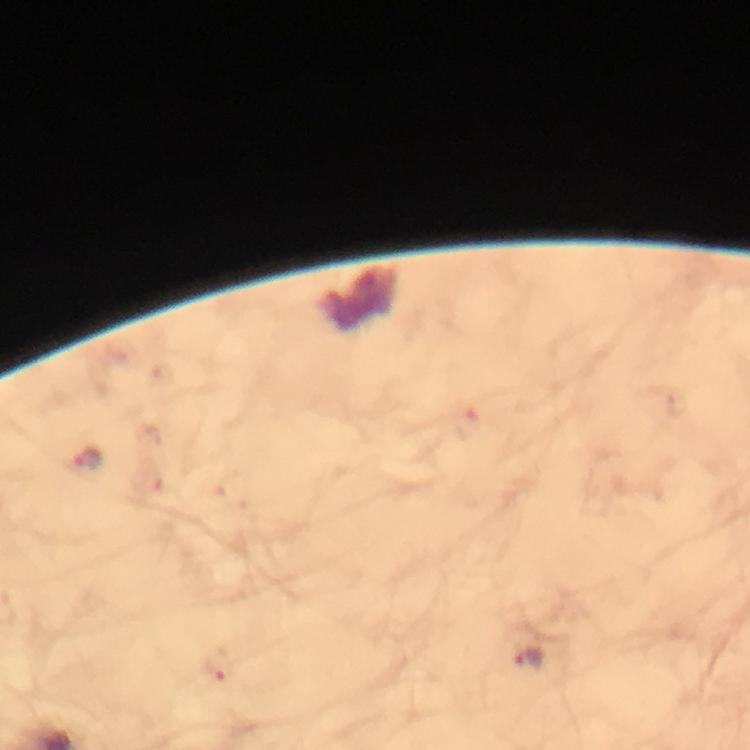

Approximate centers as [x, y] in pixels.
Summary:
  - Malaria parasite locations: [468, 426], [88, 460], [528, 658], [219, 663]
  - Cropped from: one field of view
  - Magnification: 100x
  - Preparation: thick blood smear
  - Image size: 750×750 pixels
  - Capture: smartphone camera through the microscope
  - Immersion oil: used
  - Context: from a malaria diagnostic workup
  - Stain: Giemsa